Locate every malaria parasite.
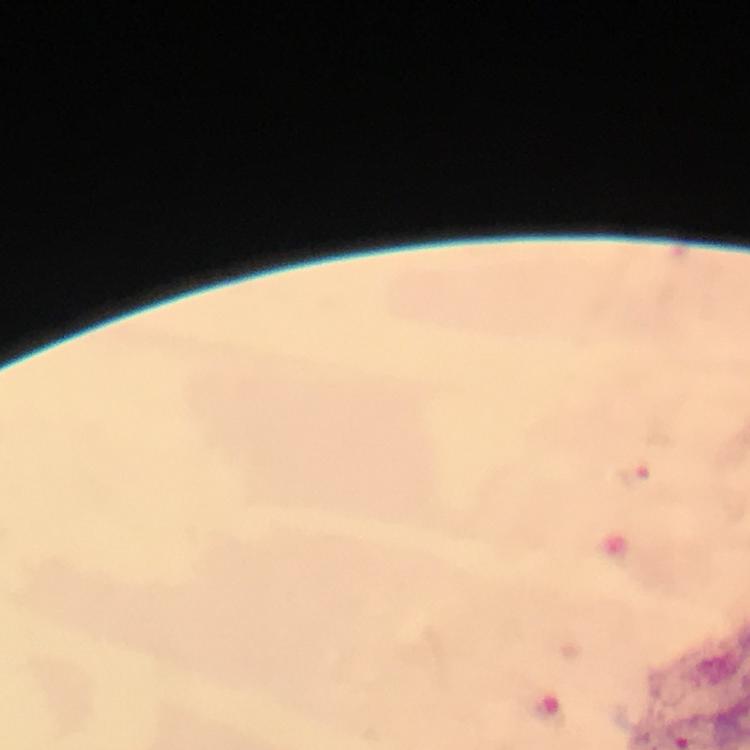

Approximate centers as {x, y} in pixels.
Malaria parasites: {634, 476}.

capture = smartphone camera through the microscope
context = from a diagnostic examination for malaria
stain = Giemsa
image size = 750×750 pixels
magnification = 100x
cropped from = one field of view
immersion oil = used
preparation = thick blood smear